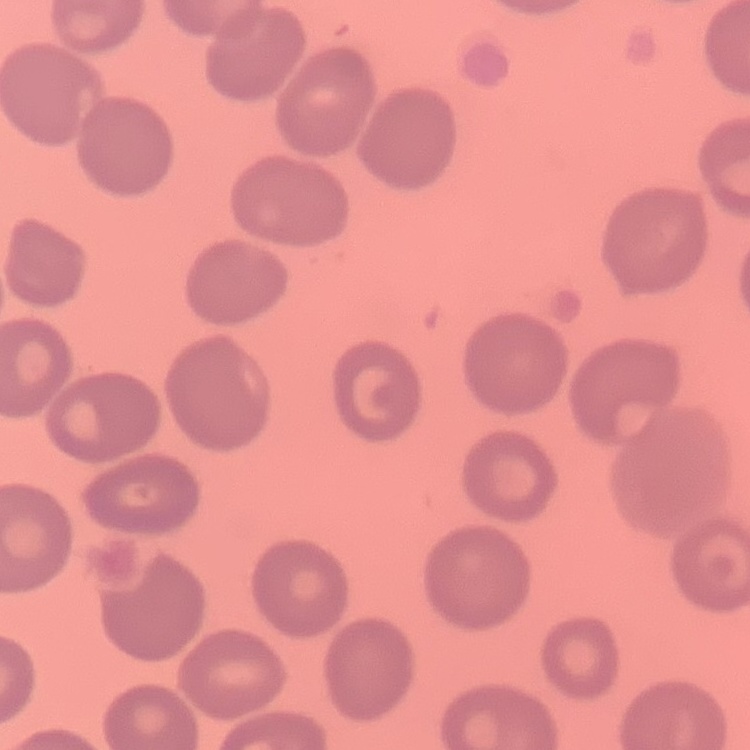

Summary:
  - Red blood cell morphology: no rouleaux formation
  - Image type: square crop of a larger photomicrograph
  - Stain: Field's or Giemsa
  - Preparation: thin blood smear